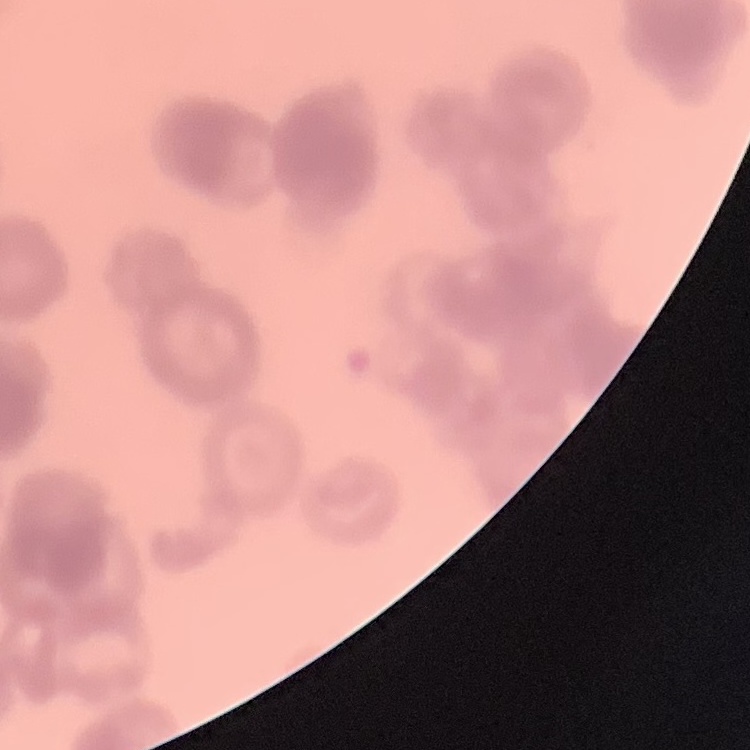

Summary:
  - Red blood cell morphology: rouleaux formation
  - Preparation: thin peripheral smear
  - Stain: Field's or Giemsa
  - Image type: one tile cut from a larger photomicrograph